State the preparation type.
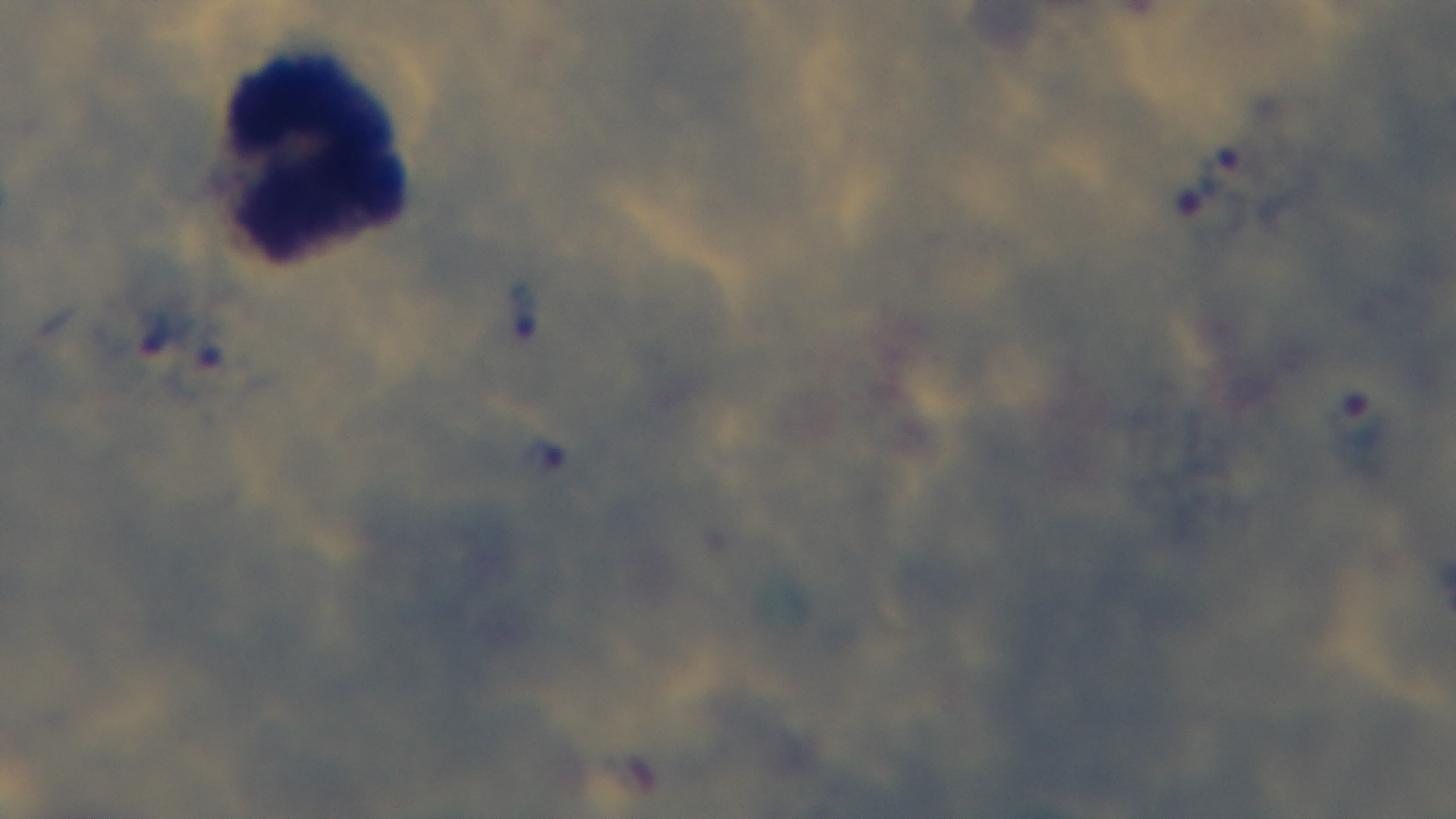

Thick.

Giemsa stain. Single field of view. Captured with a mounted 4K digital camera. Photomicrograph. Malaria status: infected. 100x oil-immersion objective.